Outline each Trypanosoma brucei.
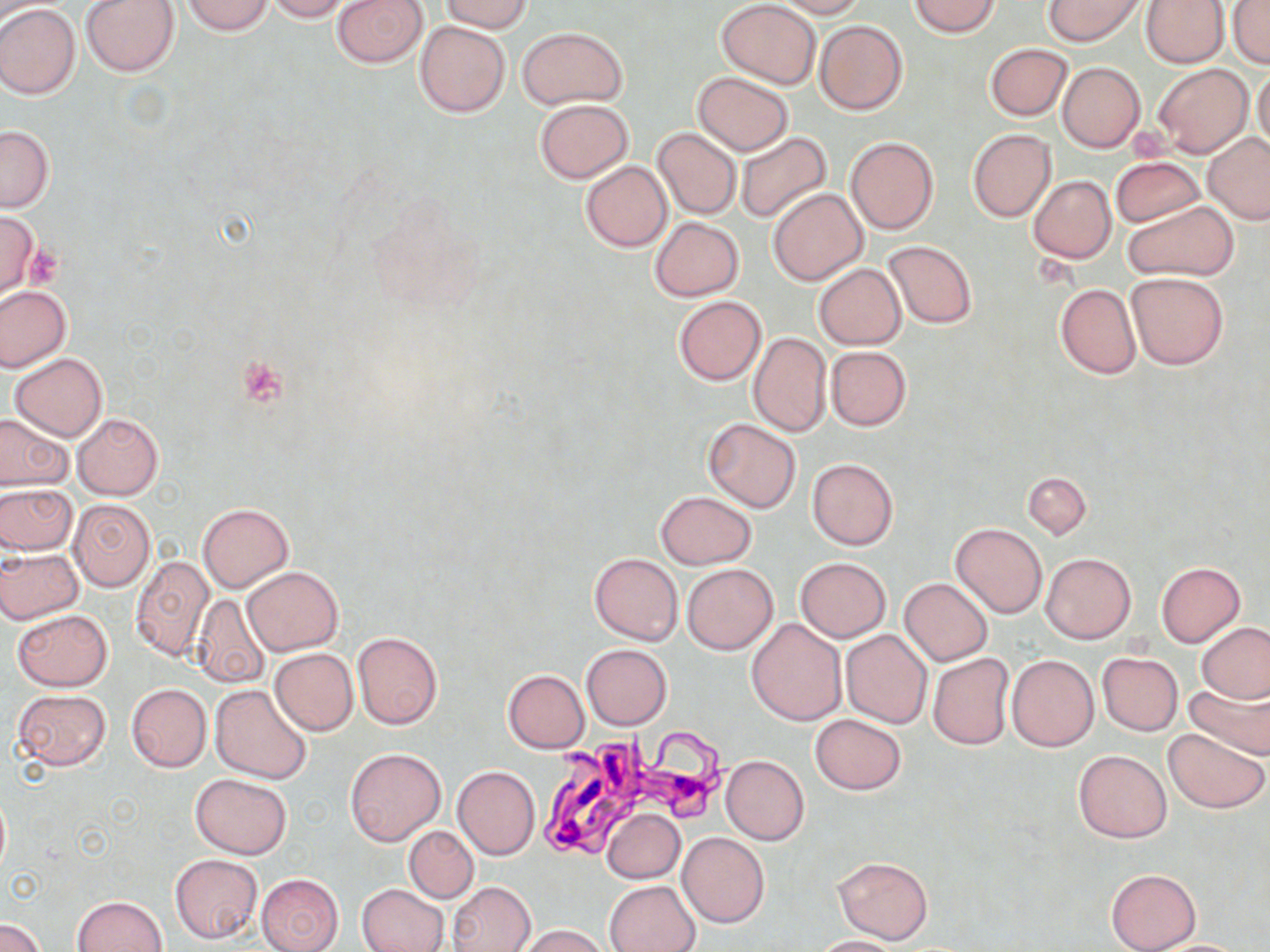

Approximate bounding boxes as named x1/y1/x2/y2 corners in pixels.
Trypanosoma brucei: (x1=540, y1=724, x2=745, y2=863).

Platelet locations: (x1=24, y1=244, x2=63, y2=288), (x1=239, y1=357, x2=288, y2=406). Uninfected red blood cell locations: (x1=81, y1=0, x2=178, y2=76), (x1=182, y1=0, x2=274, y2=35), (x1=264, y1=0, x2=352, y2=22), (x1=331, y1=0, x2=427, y2=69), (x1=439, y1=0, x2=532, y2=33), (x1=716, y1=0, x2=820, y2=88), (x1=770, y1=0, x2=868, y2=17), (x1=909, y1=0, x2=1001, y2=37), (x1=1042, y1=0, x2=1147, y2=46), (x1=1143, y1=0, x2=1228, y2=67), (x1=1229, y1=1, x2=1270, y2=69), (x1=0, y1=5, x2=81, y2=99), (x1=814, y1=19, x2=908, y2=116), (x1=415, y1=20, x2=510, y2=118), (x1=517, y1=26, x2=628, y2=109), (x1=985, y1=43, x2=1072, y2=121), (x1=1057, y1=62, x2=1145, y2=153), (x1=1153, y1=63, x2=1252, y2=157), (x1=1251, y1=65, x2=1270, y2=156), (x1=692, y1=71, x2=793, y2=155), (x1=534, y1=99, x2=634, y2=183), (x1=0, y1=126, x2=53, y2=211), (x1=652, y1=127, x2=742, y2=220), (x1=967, y1=129, x2=1056, y2=222), (x1=736, y1=131, x2=832, y2=223), (x1=1202, y1=133, x2=1270, y2=224), (x1=846, y1=137, x2=940, y2=235), (x1=1111, y1=156, x2=1204, y2=228), (x1=579, y1=161, x2=673, y2=252), (x1=1028, y1=175, x2=1116, y2=263), (x1=768, y1=187, x2=868, y2=285), (x1=1123, y1=201, x2=1239, y2=281), (x1=0, y1=212, x2=40, y2=298), (x1=648, y1=217, x2=745, y2=301), (x1=882, y1=241, x2=977, y2=328), (x1=815, y1=264, x2=906, y2=349), (x1=1126, y1=272, x2=1228, y2=370), (x1=1055, y1=284, x2=1140, y2=378), (x1=0, y1=286, x2=71, y2=373), (x1=673, y1=296, x2=766, y2=385), (x1=747, y1=332, x2=831, y2=437), (x1=825, y1=346, x2=912, y2=430), (x1=10, y1=353, x2=108, y2=440), (x1=0, y1=411, x2=72, y2=491), (x1=72, y1=413, x2=163, y2=500), (x1=702, y1=417, x2=801, y2=512), (x1=806, y1=458, x2=899, y2=550), (x1=1022, y1=471, x2=1091, y2=539), (x1=0, y1=483, x2=76, y2=555), (x1=656, y1=491, x2=755, y2=569), (x1=68, y1=500, x2=154, y2=591), (x1=198, y1=502, x2=293, y2=593), (x1=950, y1=523, x2=1046, y2=617), (x1=0, y1=547, x2=83, y2=624), (x1=589, y1=553, x2=683, y2=645), (x1=1041, y1=553, x2=1135, y2=642), (x1=130, y1=555, x2=215, y2=662), (x1=795, y1=557, x2=891, y2=642), (x1=681, y1=562, x2=779, y2=655), (x1=1154, y1=562, x2=1246, y2=646), (x1=243, y1=566, x2=343, y2=655), (x1=900, y1=577, x2=993, y2=666), (x1=188, y1=594, x2=271, y2=689), (x1=12, y1=608, x2=113, y2=690), (x1=747, y1=618, x2=846, y2=725), (x1=1197, y1=622, x2=1270, y2=704), (x1=841, y1=629, x2=932, y2=729), (x1=352, y1=631, x2=442, y2=729), (x1=582, y1=644, x2=672, y2=730), (x1=269, y1=649, x2=358, y2=736), (x1=1097, y1=652, x2=1183, y2=737), (x1=927, y1=653, x2=1014, y2=749), (x1=1006, y1=654, x2=1099, y2=751), (x1=502, y1=669, x2=589, y2=752), (x1=1184, y1=678, x2=1270, y2=757), (x1=126, y1=684, x2=211, y2=771), (x1=210, y1=684, x2=314, y2=784), (x1=11, y1=688, x2=112, y2=771), (x1=810, y1=714, x2=907, y2=795), (x1=1163, y1=727, x2=1269, y2=814), (x1=346, y1=747, x2=445, y2=846), (x1=1073, y1=749, x2=1171, y2=842), (x1=722, y1=755, x2=809, y2=845), (x1=452, y1=765, x2=539, y2=859), (x1=190, y1=773, x2=293, y2=858), (x1=0, y1=788, x2=10, y2=881), (x1=601, y1=808, x2=685, y2=883), (x1=404, y1=826, x2=478, y2=903), (x1=677, y1=831, x2=770, y2=927), (x1=169, y1=854, x2=264, y2=945), (x1=833, y1=856, x2=933, y2=944), (x1=1105, y1=867, x2=1200, y2=951), (x1=257, y1=873, x2=344, y2=952), (x1=604, y1=880, x2=701, y2=952), (x1=448, y1=881, x2=536, y2=952), (x1=356, y1=884, x2=448, y2=952), (x1=71, y1=895, x2=169, y2=952), (x1=1, y1=917, x2=45, y2=952), (x1=514, y1=924, x2=612, y2=952), (x1=808, y1=935, x2=903, y2=951), (x1=1142, y1=938, x2=1257, y2=951). Slide-level diagnosis: Trypanosoma brucei. May-Grünwald-Giemsa-stained preparation. One field of a larger specimen. Optical microscopy. Thin blood film. Image is 1270×952 pixels. Captured at 1000x magnification.